Locate every blood parasite and identify its species.
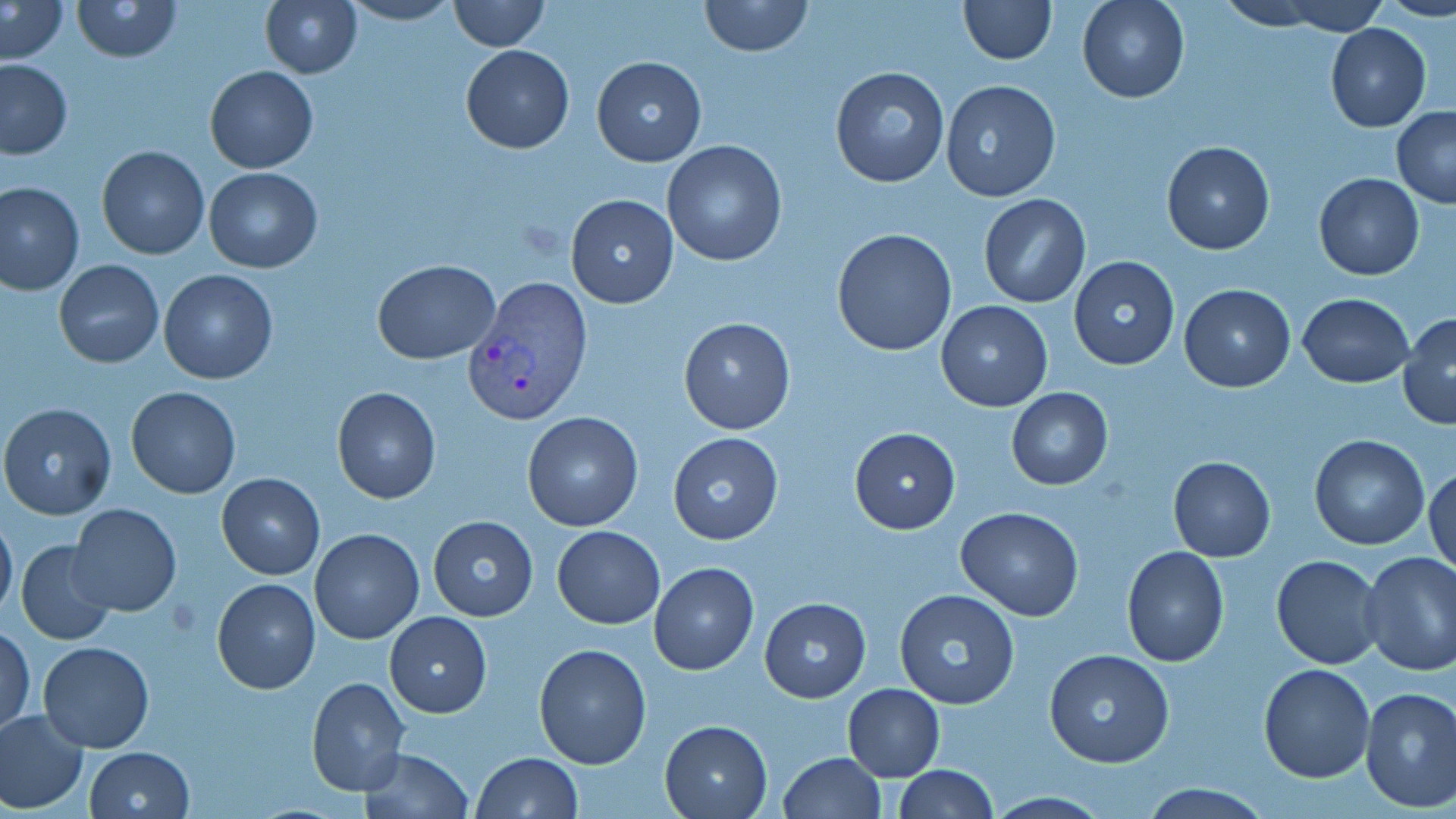
Approximate bounding boxes as [x1, y1, x2, y2] in pixels.
Plasmodium vivax-infected red blood cells: [462, 279, 589, 426].
No Plasmodium falciparum, Plasmodium ovale, Plasmodium malariae, Babesia divergens, or Trypanosoma brucei observed.

Summary:
  - Uninfected red blood cell locations: [71, 0, 183, 62], [259, 0, 363, 79], [446, 0, 548, 51], [699, 0, 813, 58], [956, 0, 1056, 64], [1077, 0, 1189, 104], [1212, 0, 1340, 32], [1270, 0, 1392, 36], [1, 1, 69, 63], [338, 1, 462, 26], [1324, 24, 1430, 131], [459, 45, 574, 154], [591, 55, 705, 166], [0, 58, 73, 159], [828, 65, 949, 187], [205, 66, 318, 173], [940, 80, 1061, 202], [1392, 106, 1456, 209], [1160, 139, 1276, 255], [661, 140, 787, 266], [96, 145, 210, 260], [204, 166, 321, 272], [1314, 173, 1425, 280], [0, 181, 85, 296], [565, 194, 678, 308], [977, 194, 1091, 307], [831, 227, 959, 357], [1068, 256, 1181, 372], [55, 259, 163, 368], [373, 259, 500, 365], [158, 269, 278, 384], [1177, 284, 1296, 393], [1295, 292, 1415, 387], [935, 300, 1053, 412], [1398, 311, 1456, 430], [679, 317, 796, 435], [126, 386, 241, 499], [331, 387, 441, 505], [1007, 387, 1112, 490], [0, 401, 117, 521], [521, 412, 644, 531], [849, 428, 961, 533], [667, 430, 784, 545], [1309, 434, 1431, 550], [1167, 455, 1276, 562], [1426, 462, 1456, 579], [215, 471, 325, 579], [66, 503, 183, 616], [956, 507, 1086, 620], [0, 513, 18, 625], [427, 516, 539, 621], [553, 525, 665, 628], [310, 530, 424, 645], [15, 540, 116, 645], [1122, 546, 1229, 666], [1358, 551, 1456, 675], [1271, 554, 1385, 670], [649, 561, 759, 675], [213, 578, 319, 693], [895, 590, 1021, 710], [758, 598, 871, 702], [384, 611, 491, 717], [1, 625, 35, 736], [37, 641, 156, 753], [533, 644, 652, 768], [1045, 648, 1176, 769], [1258, 664, 1374, 783], [307, 676, 409, 796], [843, 683, 946, 781], [1359, 686, 1456, 812], [0, 710, 88, 814], [660, 719, 773, 817], [84, 746, 195, 819], [359, 747, 473, 819], [778, 751, 886, 819], [470, 752, 582, 819], [892, 765, 998, 819], [1138, 784, 1275, 818]
  - Slide-level diagnosis: Plasmodium vivax
  - Magnification: 1000x
  - Image size: 1456×819 pixels
  - Modality: optical microscopy
  - Preparation: thin blood smear
  - Stain: May-Grünwald-Giemsa
  - Field of view: one of a larger specimen